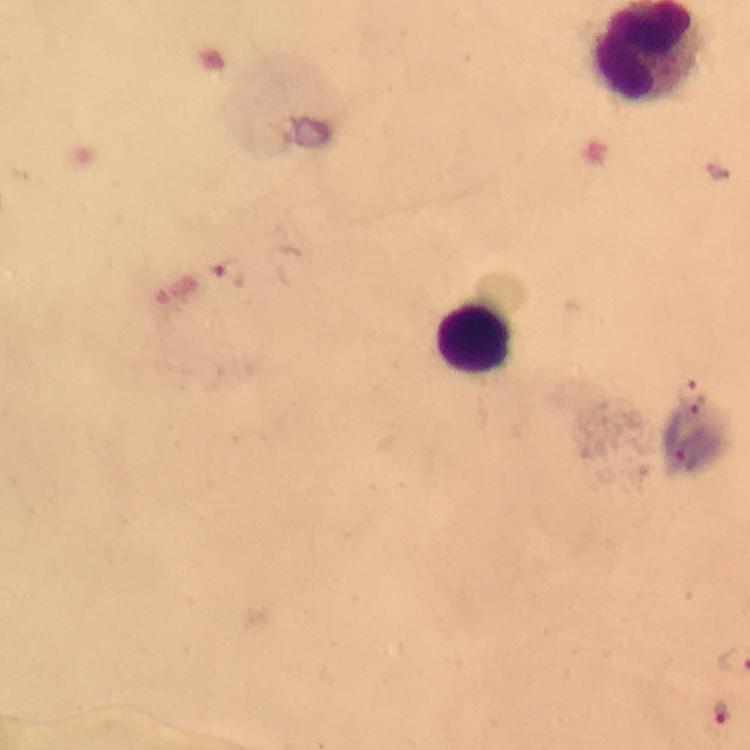

Approximate centers as (x, y) in pixels. Plasmodium parasite locations: (229, 275), (693, 396), (685, 459), (721, 712). Leukocyte locations: (473, 339). Giemsa-stained preparation. At 100x magnification. Photographed with a smartphone mounted on the microscope. Immersion oil was used. A crop from one field of view. From a malaria diagnostic workup. Thick blood film. Image is 750×750 pixels.